Identify the cell.
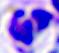
A leukocyte.

magnification = 400x
modality = photomicrograph